Report the malaria status.
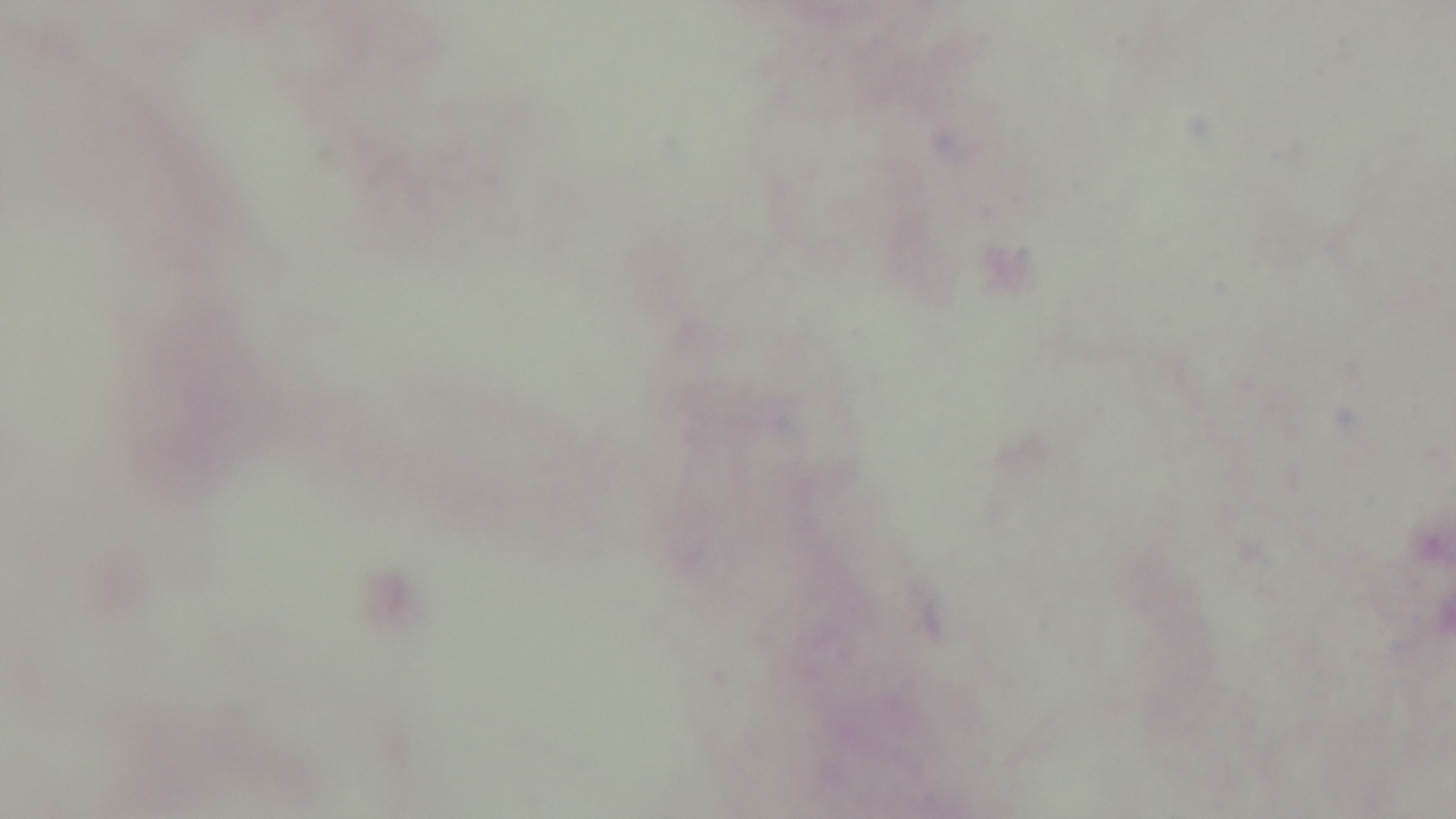

Negative.

Giemsa stain. Preparation: thick. Captured with a mounted 4K digital camera. Light microscopy. One field from the slide. 100x oil-immersion objective.